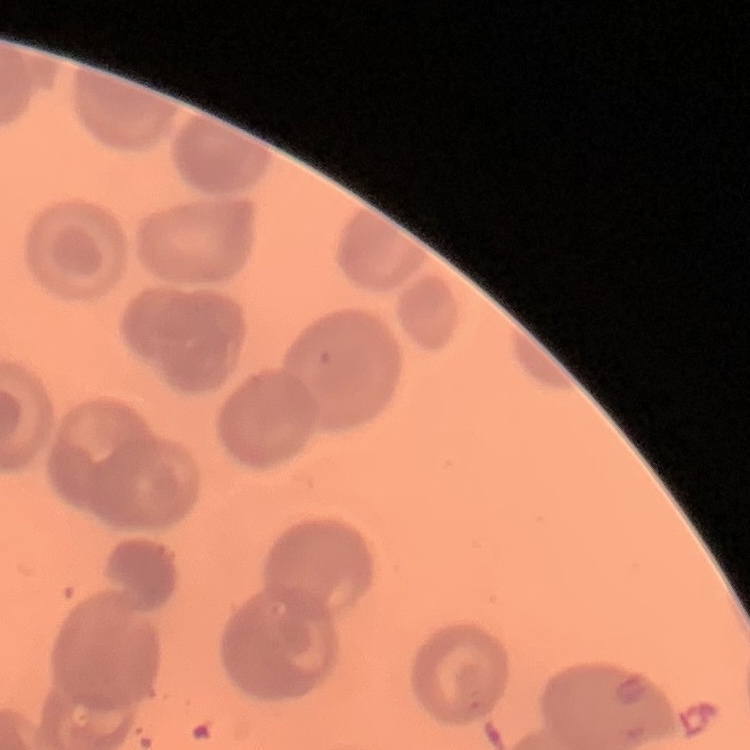 The red blood cells show no rouleaux formation. Thin peripheral smear. Square crop of a larger photomicrograph. Field's or Giemsa stain.